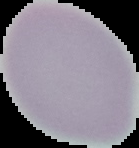 Malaria status: uninfected. The area outside the segmented cell region is set to black. From a thin blood film. Image is 139×148 pixels.